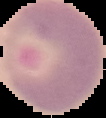 Result: no Plasmodium parasites detected. From a thin blood smear. Image is 106×118 pixels. Cell region segmented out of the field of view; the surrounding area is masked to black.